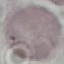 Result: negative for malaria parasites. Giemsa-stained preparation. Cell patch, automatically extracted from a larger field of view and resized to 64 × 64 pixels. Acquired by smartphone through the microscope eyepiece. Thin smear of blood.